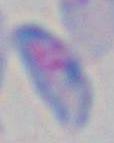

Summary:
  - Modality: micrograph
  - Identification: Toxoplasma gondii
  - Magnification: 1000x